Give the position of every Plasmodium parasite.
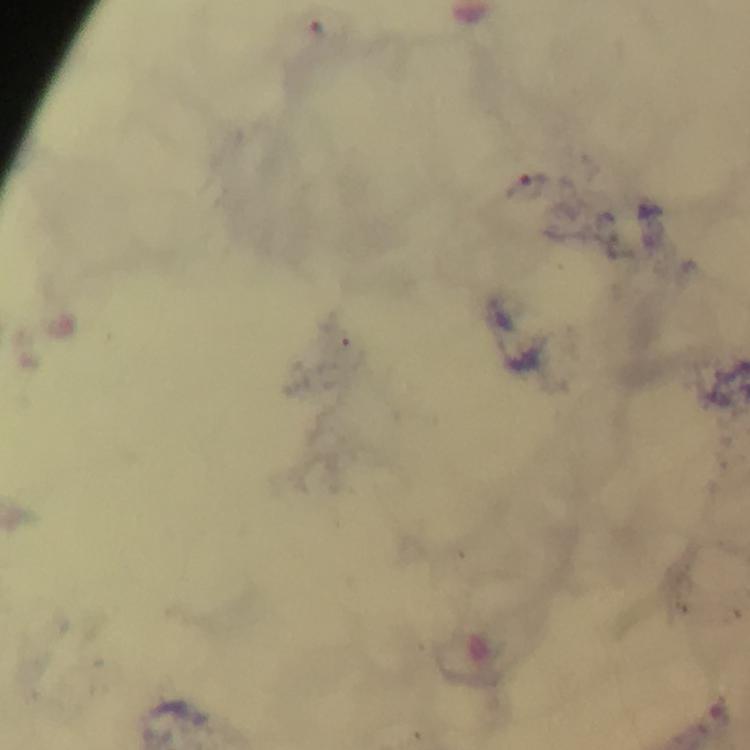
Approximate centers as {x, y} in pixels.
Plasmodium parasites: {528, 184}.

{
  "stain": "Giemsa",
  "context": "from a malaria diagnostic workup",
  "cropped_from": "a single field of view",
  "immersion_oil": "used",
  "preparation": "thick smear",
  "image_size": "750×750 pixels",
  "capture": "smartphone camera through the microscope",
  "magnification": "100x"
}